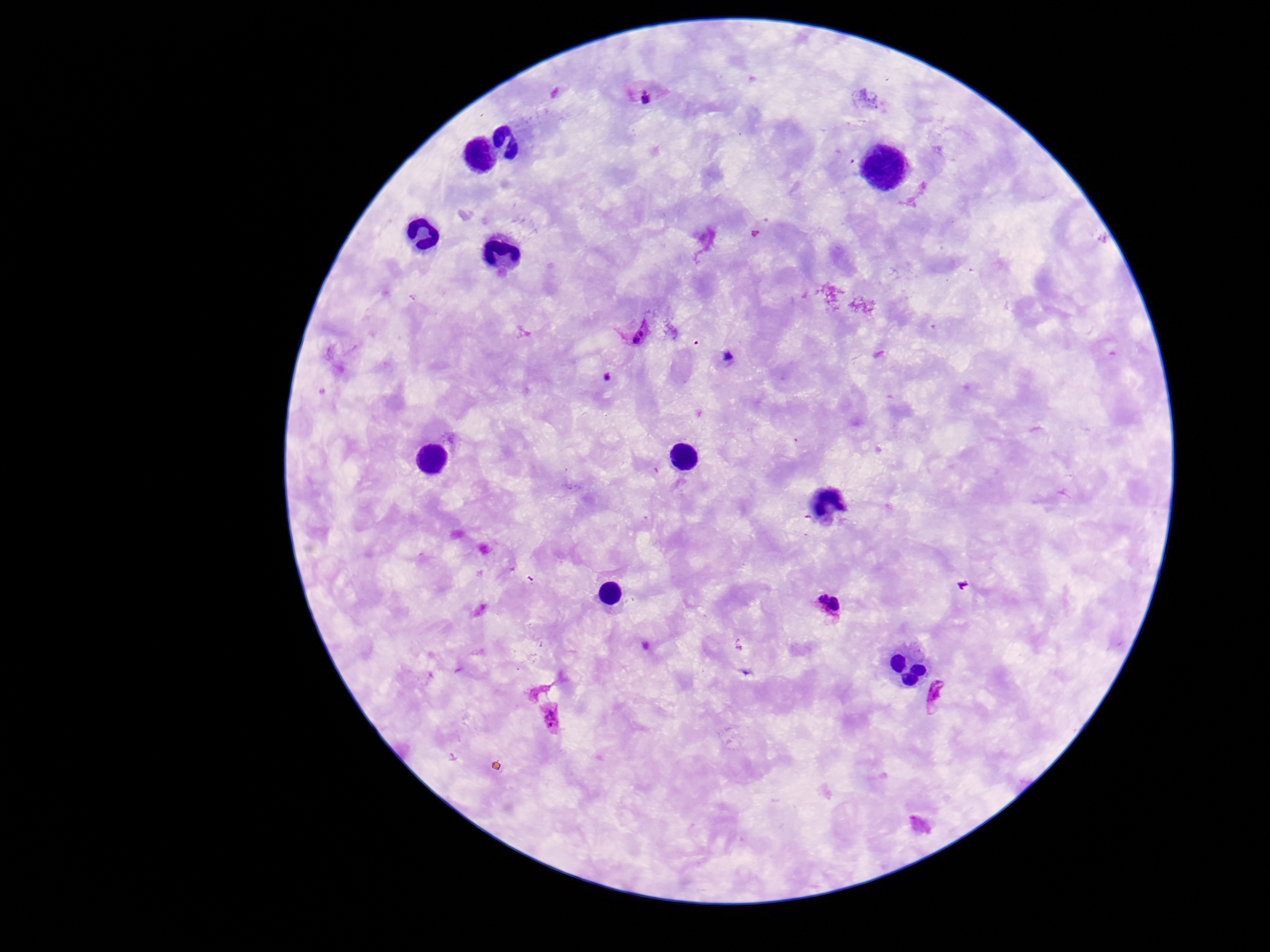
Approximate centers as {x, y} in pixels. Plasmodium parasite locations: {646, 95}, {635, 332}, {831, 605}, {941, 694}, {551, 717}. One field from this slide. 100x magnification. Patient malaria status: positive. Image is 1270×952 pixels. Thick peripheral-blood smear. Giemsa stain. Smartphone photograph taken through the microscope eyepiece.